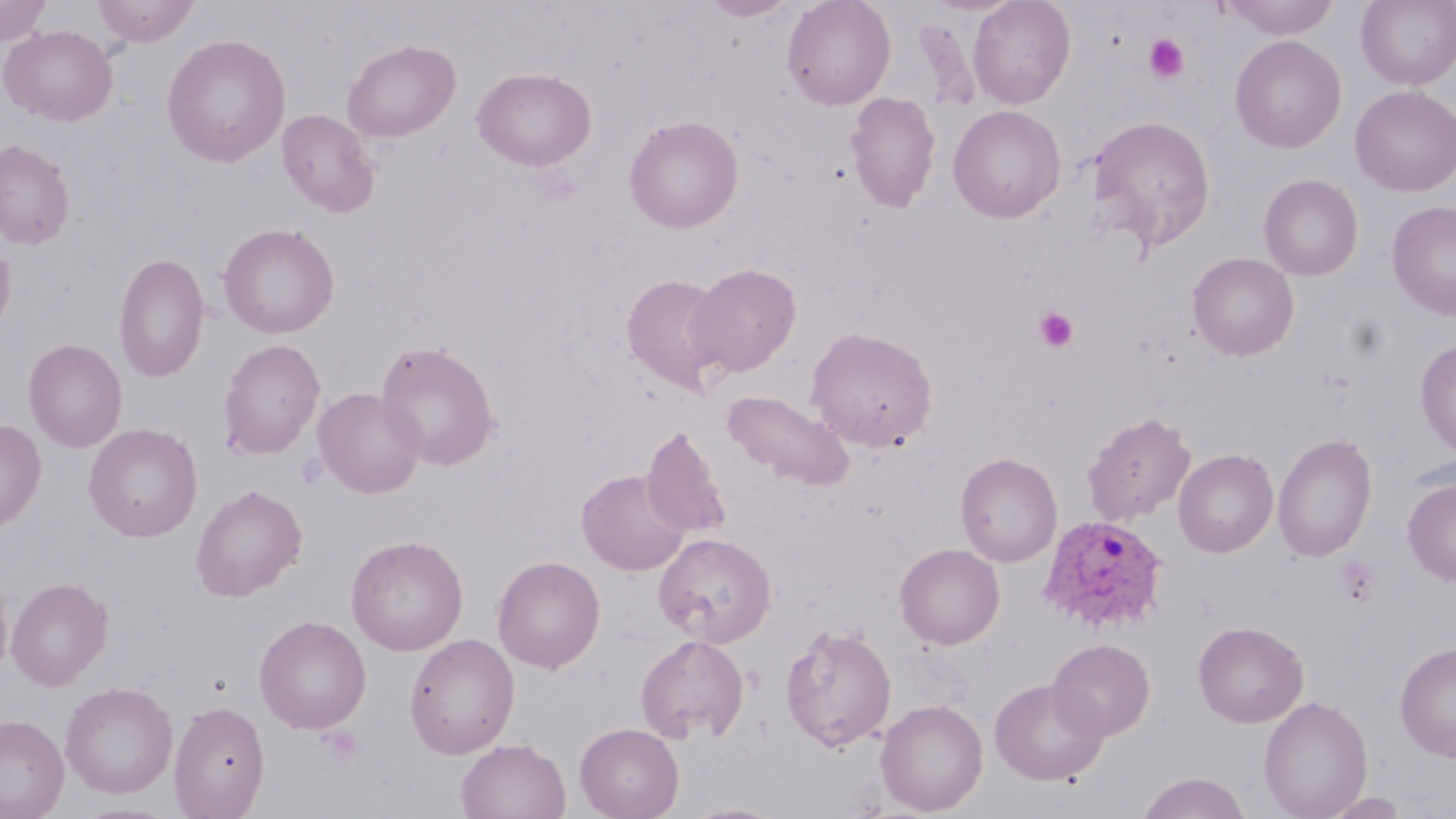

{
  "slide_level_diagnosis": "Plasmodium ovale",
  "platelet_locations": "approximate bounding boxes as (x1, y1, x2, y2) in pixels: (1143, 34, 1189, 84), (1034, 307, 1078, 352), (1335, 556, 1380, 607), (320, 726, 366, 765)",
  "image_size": "1456×819 pixels",
  "modality": "optical microscopy",
  "field_of_view": "single",
  "plasmodium_ovale_infected_red_blood_cell_locations": "approximate bounding boxes as (x1, y1, x2, y2) in pixels: (1038, 513, 1170, 634)",
  "preparation": "thin blood film",
  "stain": "May-Grünwald-Giemsa",
  "uninfected_red_blood_cell_locations": "approximate bounding boxes as (x1, y1, x2, y2) in pixels: (0, 0, 54, 46), (91, 0, 200, 47), (701, 0, 798, 21), (782, 0, 896, 111), (968, 0, 1076, 109), (1215, 0, 1344, 40), (1356, 0, 1456, 89), (1, 25, 118, 126), (161, 33, 291, 168), (1229, 35, 1346, 153), (341, 38, 461, 143), (472, 67, 596, 171), (1350, 85, 1456, 196), (845, 91, 941, 213), (948, 104, 1066, 223), (276, 108, 381, 218), (1087, 114, 1216, 252), (624, 115, 744, 233), (0, 139, 75, 249), (1259, 174, 1363, 280), (1386, 200, 1456, 321), (218, 222, 340, 339), (0, 236, 16, 340), (113, 252, 209, 383), (1187, 252, 1299, 361), (686, 263, 801, 377), (621, 274, 732, 395), (805, 326, 938, 451), (23, 338, 127, 453), (1415, 338, 1456, 458), (217, 339, 325, 459), (375, 340, 501, 471), (312, 387, 426, 499), (722, 390, 854, 491), (1082, 411, 1196, 526), (0, 417, 47, 534), (83, 423, 203, 542), (642, 425, 731, 540), (1273, 432, 1377, 561), (1173, 448, 1278, 558), (955, 451, 1062, 567), (576, 469, 690, 576), (1403, 479, 1456, 587), (190, 483, 308, 602), (653, 532, 776, 647), (346, 534, 468, 655), (895, 543, 1005, 649), (492, 555, 605, 673), (0, 570, 13, 684), (6, 576, 113, 690), (254, 614, 372, 734), (1193, 621, 1308, 728), (780, 623, 896, 752), (404, 633, 520, 759), (635, 635, 749, 743), (1047, 638, 1155, 741), (1394, 641, 1456, 761), (989, 679, 1108, 786), (60, 681, 178, 799), (1258, 695, 1374, 818), (876, 698, 988, 816), (169, 700, 270, 818), (0, 713, 69, 819), (575, 722, 684, 819), (455, 738, 571, 819), (1136, 771, 1252, 819), (1324, 792, 1409, 818), (681, 801, 790, 819)",
  "magnification": "1000x"
}